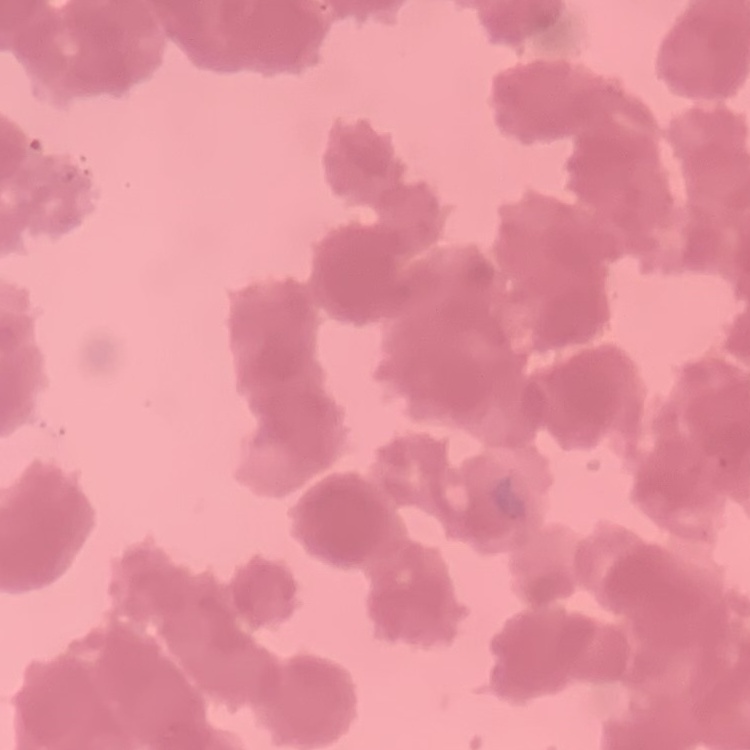
erythrocyte morphology = rouleaux formation
preparation = thin peripheral smear
stain = Field's or Giemsa
image type = one tile cut from a larger photomicrograph